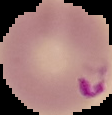

Summary:
  - Malaria status: parasitized
  - Image type: cell region segmented out of the field of view; surrounding area masked to black
  - Image size: 112×115 pixels
  - Preparation: thin blood film